Report the malaria status.
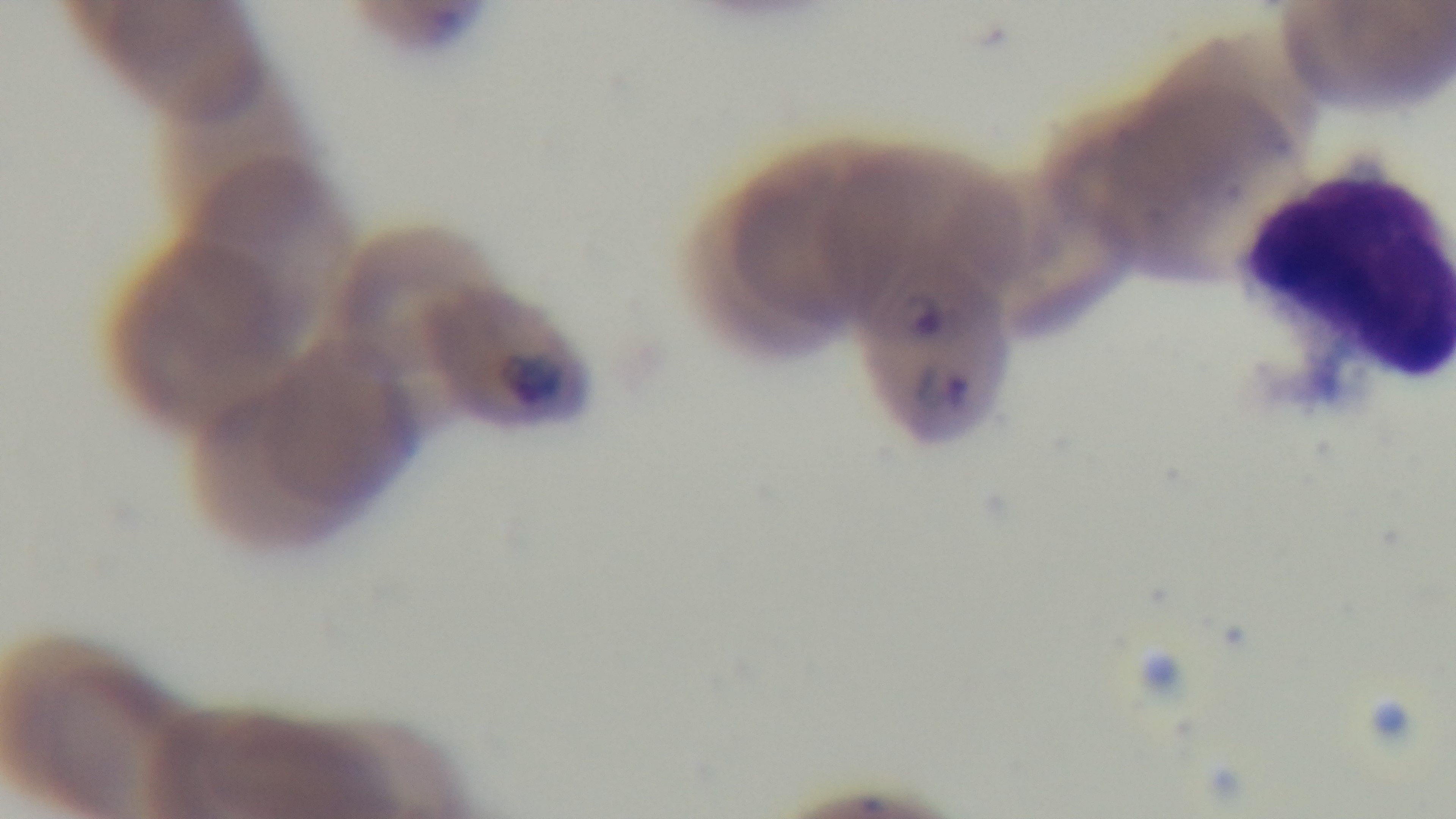
Infected.

field of view = single
objective = 100x oil immersion
stain = Giemsa
preparation = thin blood film
modality = light microscopy
capture = mounted 4K digital camera